Comment on the morphology of the erythrocytes.
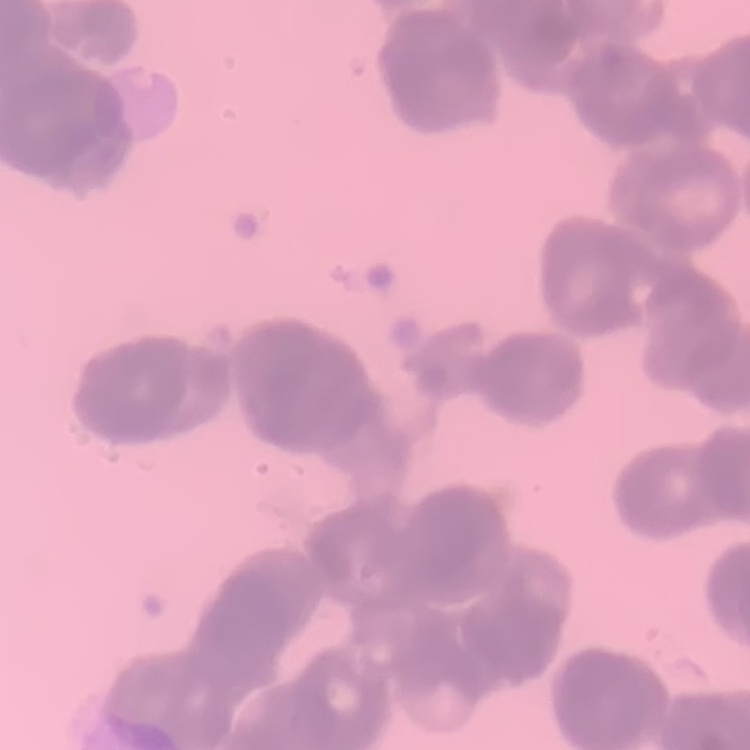
They show rouleaux formation.

Summary:
  - Stain: Field's or Giemsa
  - Preparation: thin blood smear
  - Image type: one tile cut from a larger photomicrograph